Assess this cell for malaria.
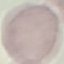
It is uninfected.

Giemsa stain. Acquired by smartphone through the microscope eyepiece. Thin blood smear. Cell patch, automatically extracted from a larger field of view and resized to 64 × 64 pixels.